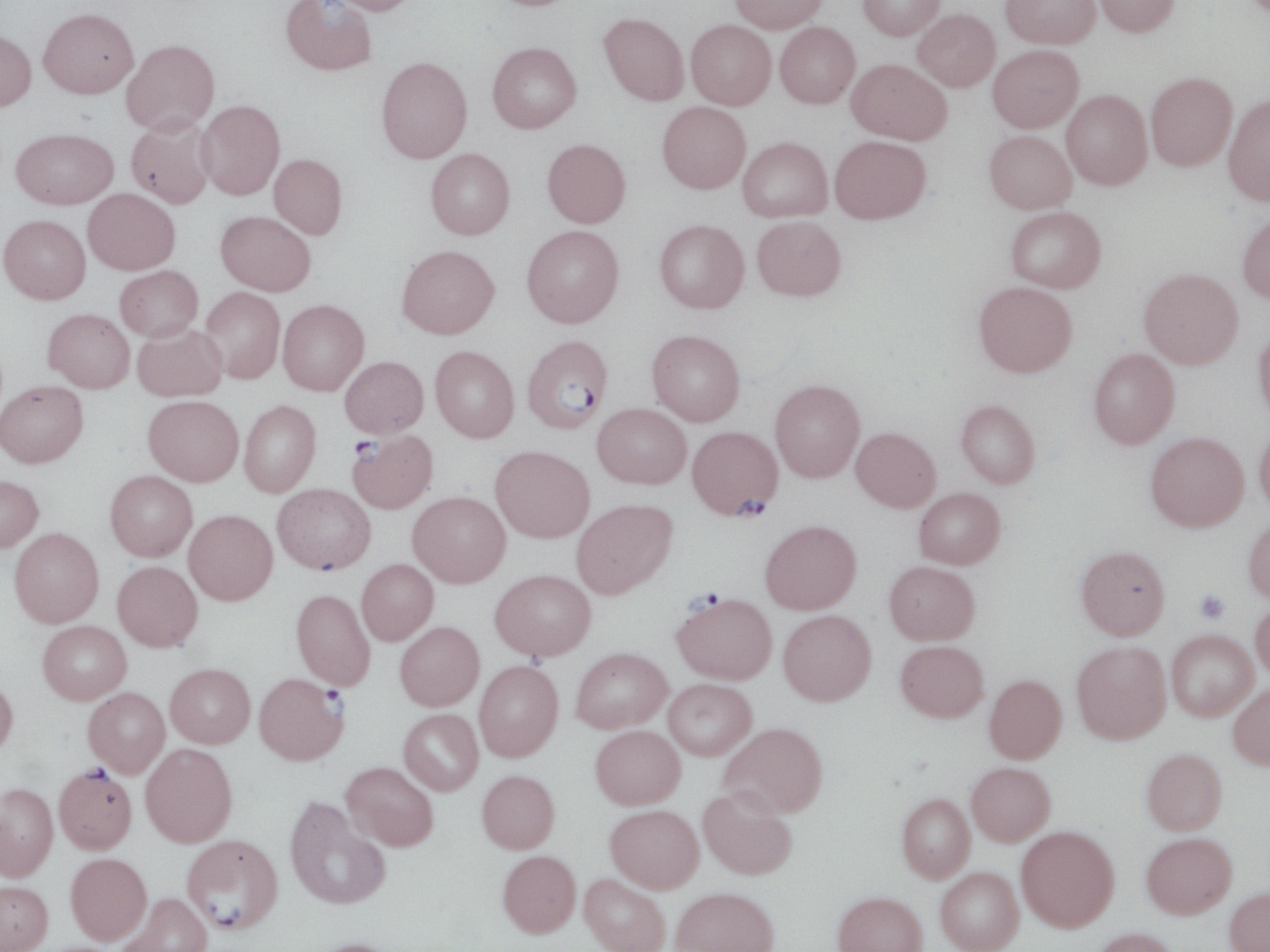
Approximate bounding boxes as (x1,y1)-(x2,y2) corner pairs in pixels. Platelet locations: (1194,590)-(1230,623). Uninfected red blood cell locations: (325,0)-(421,16), (729,0)-(828,34), (857,0)-(945,41), (1000,0)-(1100,48), (1092,0)-(1180,37), (280,1)-(377,77), (38,7)-(139,98), (912,9)-(1000,91), (599,12)-(689,106), (686,20)-(776,110), (774,22)-(860,108), (0,28)-(36,112), (121,39)-(219,136), (487,42)-(581,134), (988,44)-(1083,132), (376,56)-(472,163), (847,58)-(952,145), (1146,72)-(1237,171), (1061,89)-(1153,190), (1223,94)-(1270,206), (196,100)-(285,201), (657,101)-(750,193), (126,116)-(216,210), (11,128)-(118,209), (984,130)-(1077,213), (738,136)-(832,222), (829,136)-(931,224), (542,138)-(631,228), (425,148)-(515,240), (269,154)-(347,240), (83,188)-(180,275), (1005,206)-(1106,293), (215,211)-(315,297), (1237,212)-(1270,304), (0,215)-(90,306), (752,215)-(846,301), (654,219)-(749,313), (522,225)-(624,328), (396,245)-(499,339), (115,266)-(202,342), (1139,268)-(1243,369), (973,281)-(1077,377), (200,286)-(285,384), (278,300)-(369,396), (43,309)-(135,393), (132,324)-(227,402), (1253,326)-(1270,424), (646,329)-(745,426), (430,346)-(519,442), (1088,349)-(1180,449), (339,356)-(428,438), (770,379)-(865,482), (0,380)-(88,468), (143,395)-(243,486), (239,400)-(321,497), (956,400)-(1041,488), (593,403)-(691,488), (1254,421)-(1270,514), (851,427)-(941,512), (1145,432)-(1248,531), (490,445)-(594,543), (105,470)-(197,561), (0,475)-(43,553), (272,483)-(375,574), (914,487)-(1005,569), (408,491)-(511,587), (571,498)-(677,599), (184,509)-(278,605), (1243,516)-(1270,603), (760,520)-(862,614), (9,527)-(104,628), (1076,546)-(1170,639), (356,559)-(438,645), (112,561)-(203,652), (884,561)-(980,645), (490,568)-(596,660), (291,589)-(376,691), (1250,600)-(1270,680), (778,609)-(876,705), (37,620)-(131,704), (395,621)-(484,711), (1166,630)-(1257,720), (895,640)-(989,722), (1071,642)-(1171,744), (571,646)-(672,732), (474,660)-(563,762), (165,662)-(255,748), (984,674)-(1067,763), (0,676)-(18,759), (662,678)-(757,760), (1228,683)-(1270,770), (83,687)-(170,777), (399,708)-(483,795), (720,722)-(828,817), (590,725)-(685,809), (140,743)-(237,847), (1142,748)-(1227,835), (341,761)-(439,851), (967,762)-(1056,845), (476,769)-(559,853), (0,782)-(58,880), (698,786)-(797,879), (896,793)-(975,882), (285,796)-(390,910), (605,804)-(704,892), (1016,826)-(1119,931), (1141,832)-(1237,918), (497,850)-(581,937), (65,853)-(151,944), (936,867)-(1024,952), (579,874)-(670,952), (0,880)-(52,951), (670,887)-(779,952), (1225,887)-(1270,952), (832,891)-(928,952), (117,892)-(212,952), (1090,928)-(1180,952), (307,937)-(406,952). Plasmodium falciparum-infected red blood cell locations: (522,336)-(612,435), (687,425)-(782,520), (347,430)-(438,514), (673,592)-(777,684), (254,673)-(347,765), (53,765)-(137,853), (181,833)-(282,932). Slide-level diagnosis: Plasmodium falciparum. Single field of view. Optical microscopy. 1000x magnification. Image is 1270×952 pixels. May-Grünwald-Giemsa stain. Thin blood film.